Locate malaria parasites and leukocytes.
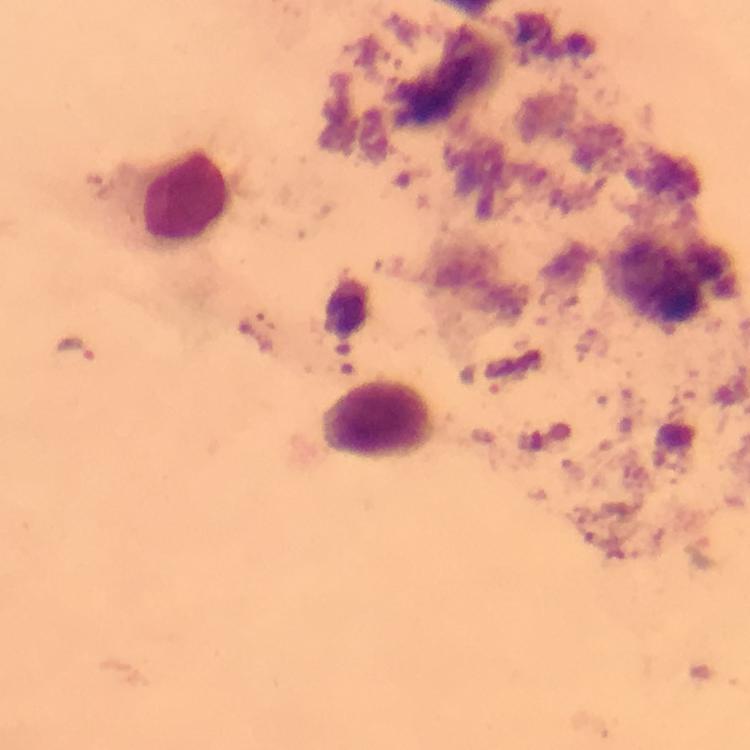
Approximate object centers, in pixels from the top-left corner.
Malaria parasites: (x=73, y=348).
Leukocytes: (x=187, y=196), (x=377, y=417).

context = from a diagnostic examination for malaria
cropped from = one field of view
stain = Giemsa
preparation = thick blood smear
immersion oil = applied
magnification = 100x
image size = 750×750 pixels
capture = smartphone mounted on the microscope